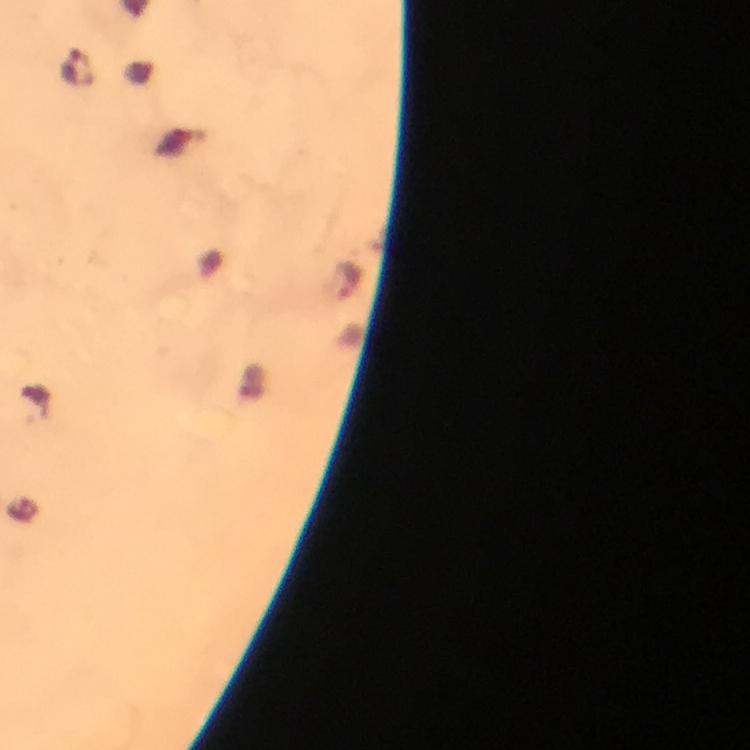 Approximate centers as [x, y] in pixels. Plasmodium parasite locations: [75, 65], [347, 281]. Photographed through the microscope with a smartphone camera. At 100x magnification. Immersion oil was used. From a malaria diagnostic workup. Thick blood film. Cropped region of a single field of view. Giemsa-stained preparation. Image is 750×750 pixels.